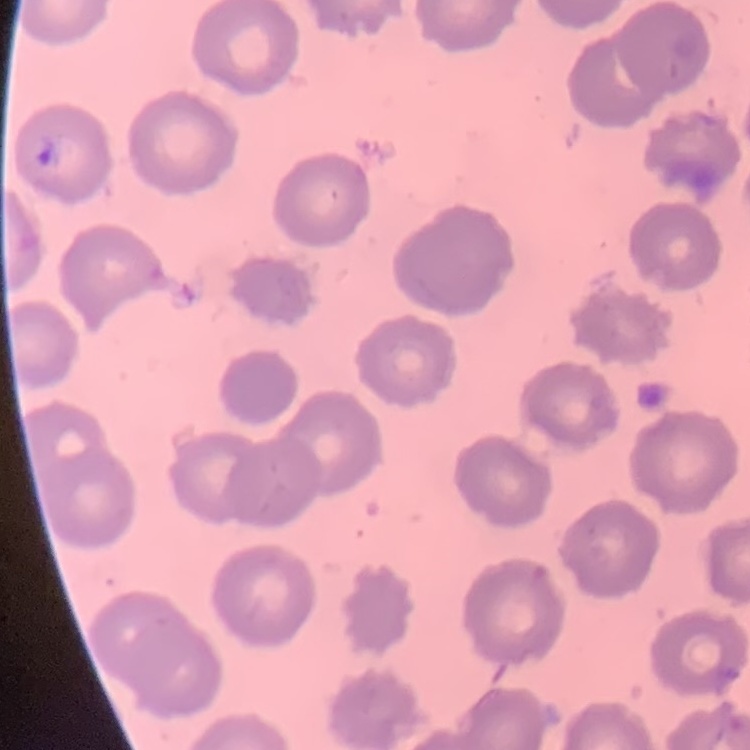
The erythrocytes show no rouleaux formation. Thin blood smear. Field's or Giemsa stain. One tile cut from a larger photomicrograph.